Locate every blood parasite and identify its species.
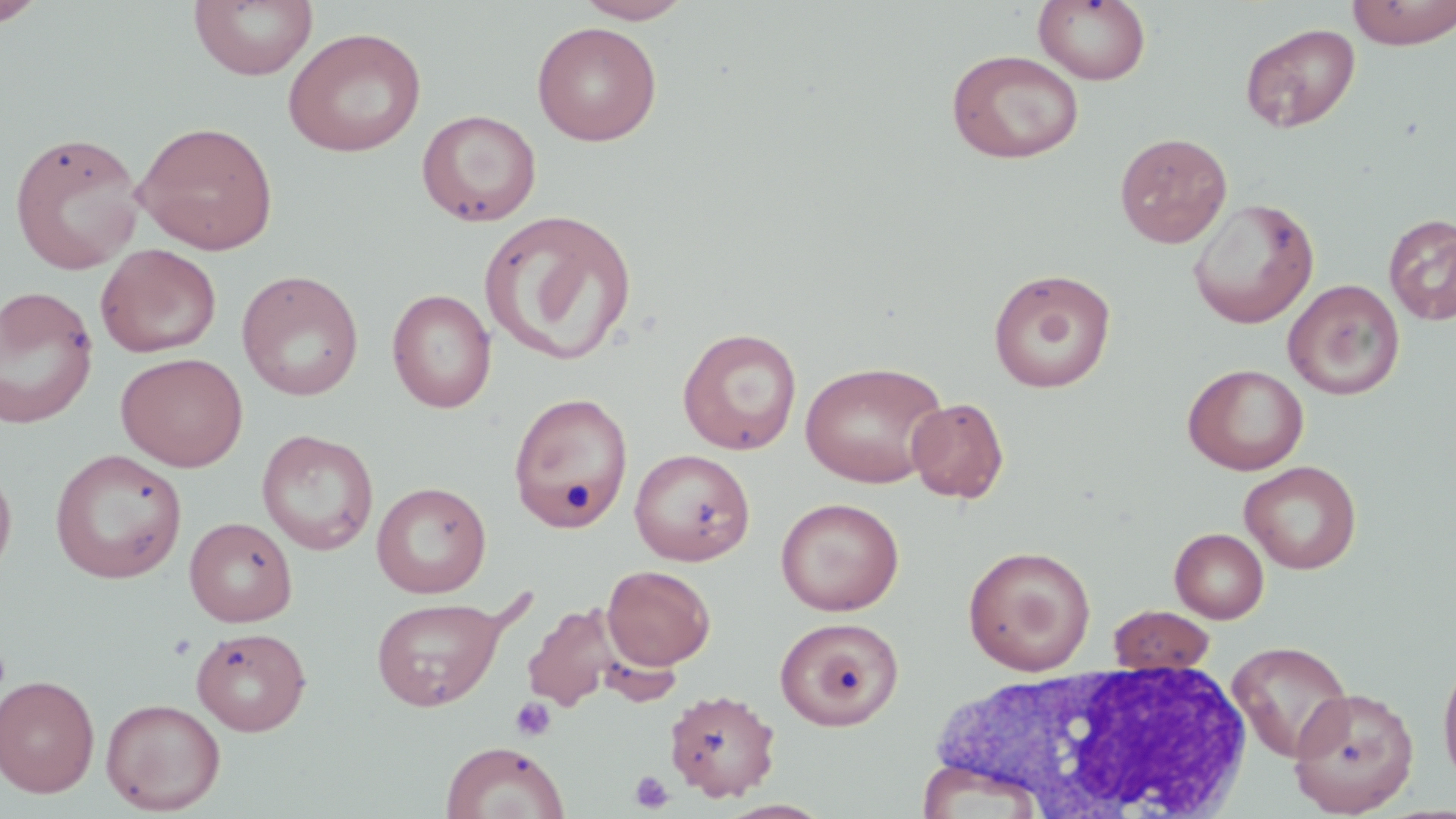

No blood parasites observed.

Approximate bounding boxes as (x1, y1, x2, y2) in pixels. Uninfected red blood cell locations: (188, 0, 318, 82), (574, 0, 695, 24), (1033, 0, 1152, 85), (1346, 0, 1456, 48), (1, 1, 49, 26), (531, 21, 662, 146), (1239, 22, 1361, 133), (282, 26, 427, 158), (946, 49, 1085, 164), (416, 109, 542, 227), (133, 119, 278, 255), (8, 131, 146, 275), (1114, 132, 1233, 249), (1186, 197, 1320, 329), (479, 209, 638, 366), (1383, 215, 1456, 325), (96, 243, 221, 358), (988, 268, 1116, 394), (237, 270, 364, 401), (1283, 279, 1405, 400), (0, 286, 99, 429), (386, 288, 497, 413), (677, 327, 802, 455), (115, 352, 249, 472), (800, 360, 948, 488), (1182, 363, 1309, 475), (508, 391, 633, 534), (906, 397, 1009, 503), (256, 429, 379, 556), (49, 448, 187, 584), (629, 448, 756, 566), (0, 457, 17, 588), (1239, 460, 1361, 574), (371, 481, 492, 598), (775, 497, 904, 616), (184, 516, 297, 626), (1170, 528, 1269, 623), (963, 545, 1096, 675), (602, 565, 716, 670), (370, 596, 507, 711), (523, 601, 622, 712), (1108, 605, 1215, 673), (775, 616, 904, 731), (192, 627, 311, 736), (1227, 640, 1354, 762), (1437, 653, 1456, 791), (0, 674, 101, 798), (1, 680, 227, 801), (1288, 686, 1419, 816), (664, 688, 781, 801), (101, 697, 226, 815), (440, 741, 569, 819). Platelet locations: (510, 697, 557, 742), (630, 770, 674, 813). White blood cell locations: (920, 666, 1260, 817). Slide-level diagnosis: negative for blood parasites. One field of a larger specimen. Thin blood film. Light microscopy. May-Grünwald-Giemsa stain. Image is 1456×819 pixels. 1000x magnification.